Describe the morphology of the red blood cells.
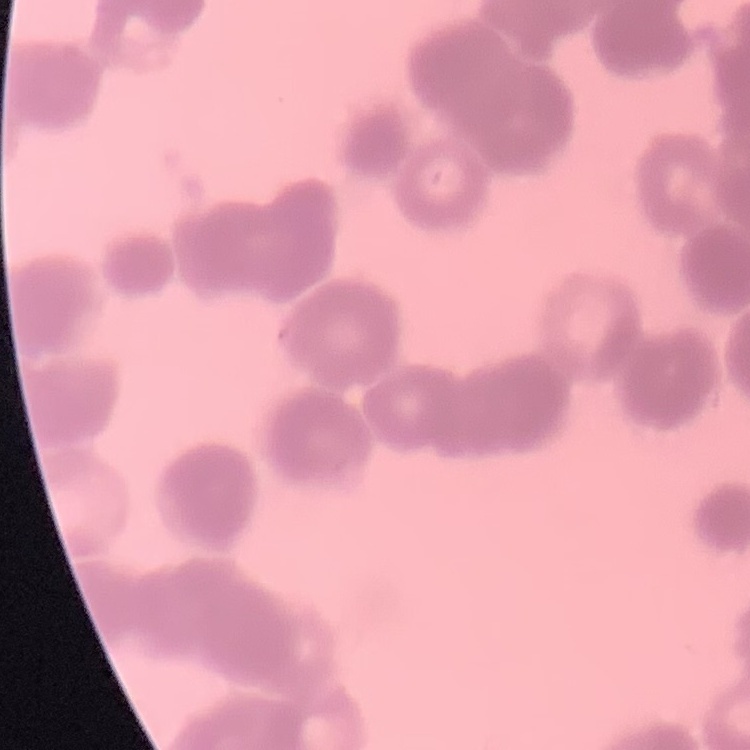

Rouleaux formation.

One tile cut from a larger photomicrograph. Stained with either Field's or Giemsa. Thin peripheral smear.